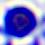

modality = photomicrograph
identification = leukocyte
magnification = 400x